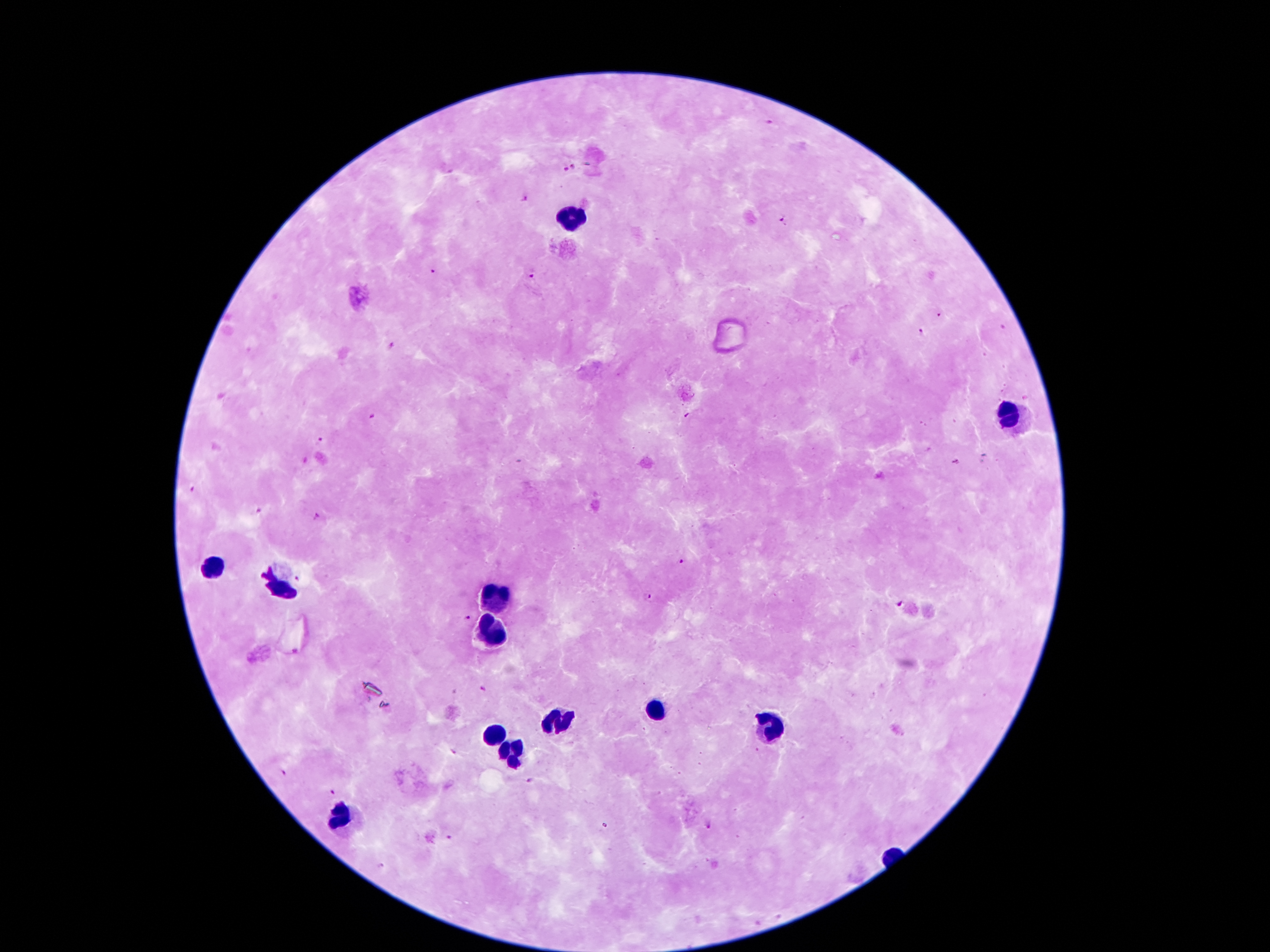 Approximate centers as {x, y} in pixels. Leukocyte locations: {569, 218}, {1007, 415}, {215, 568}, {281, 590}, {495, 595}, {488, 632}, {657, 707}, {559, 721}, {774, 725}, {493, 735}, {510, 750}, {342, 817}. Plasmodium parasite locations: {770, 122}, {572, 166}, {566, 169}, {525, 199}, {781, 221}, {433, 271}, {531, 274}, {939, 314}, {919, 332}, {392, 347}, {375, 417}, {687, 417}, {320, 440}, {956, 462}, {189, 490}, {258, 511}, {317, 517}, {683, 563}, {297, 578}, {648, 599}, {899, 604}, {467, 618}, {484, 689}, {454, 750}, {280, 774}, {529, 780}, {332, 791}, {709, 823}, {449, 837}, {382, 864}. Patient malaria status: positive for Plasmodium falciparum. Single field of view. Smartphone photograph taken through the microscope eyepiece. Giemsa stain. Image is 1270×952 pixels. 100x magnification. Thick blood film.